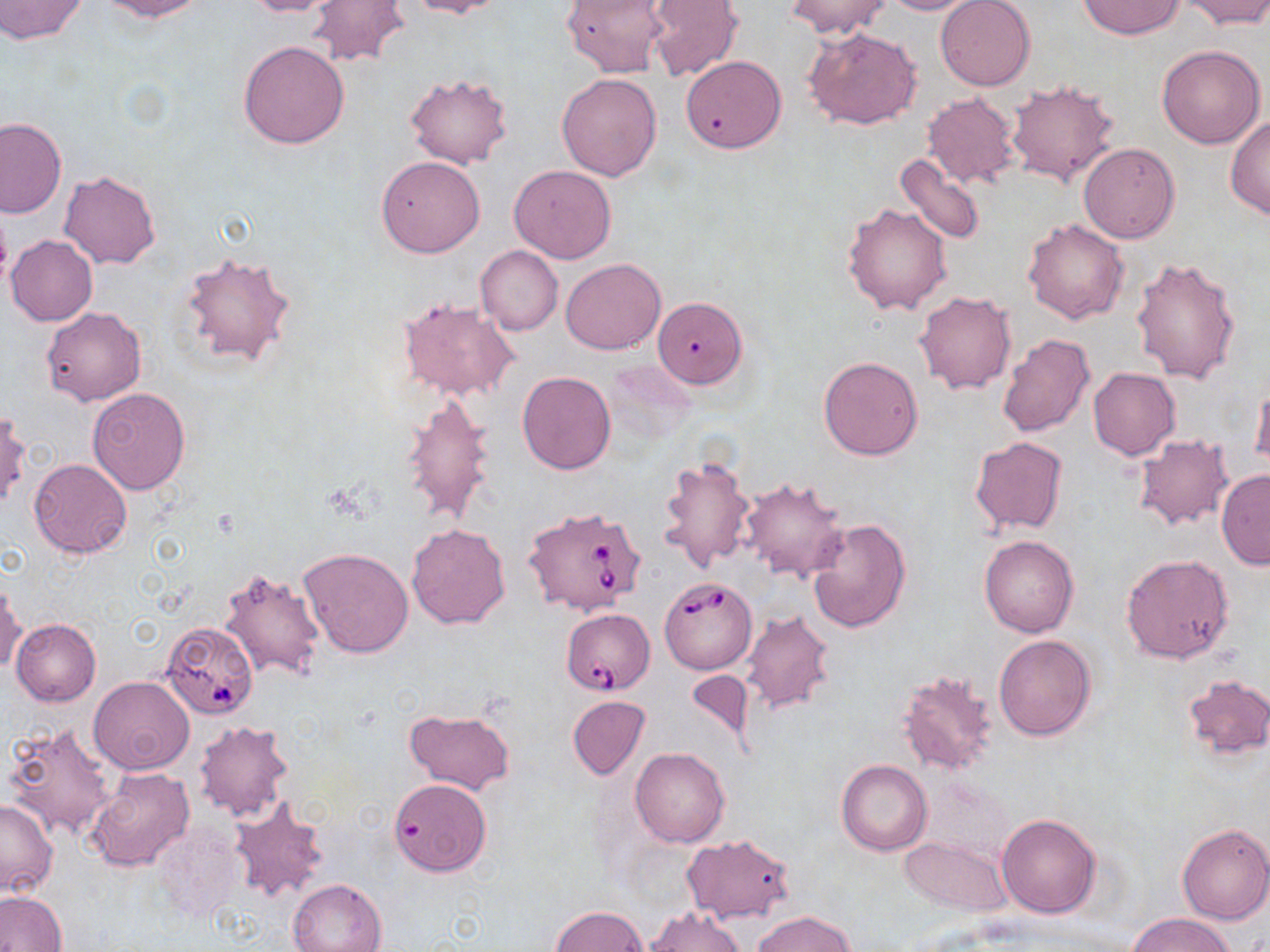

Summary:
  - Coordinate format: approximate bounding boxes as [x1, y1, x2, y2] in pixels
  - Uninfected red blood cell locations: [0, 0, 88, 44], [97, 0, 207, 21], [242, 0, 345, 17], [308, 0, 409, 67], [401, 0, 508, 19], [562, 0, 670, 77], [787, 0, 890, 38], [878, 0, 982, 14], [935, 0, 1036, 91], [1077, 0, 1185, 38], [1182, 0, 1270, 28], [645, 1, 743, 80], [805, 26, 922, 131], [237, 40, 350, 148], [1157, 45, 1265, 149], [680, 55, 786, 154], [557, 72, 663, 180], [405, 73, 514, 169], [1007, 79, 1121, 190], [921, 93, 1023, 189], [1227, 116, 1270, 221], [0, 118, 66, 218], [1079, 143, 1180, 242], [894, 151, 988, 246], [376, 156, 485, 257], [509, 164, 616, 263], [59, 171, 161, 269], [0, 202, 11, 294], [844, 203, 952, 315], [1022, 219, 1129, 324], [6, 235, 97, 326], [476, 246, 563, 335], [177, 250, 298, 371], [1131, 257, 1241, 384], [561, 259, 665, 354], [914, 291, 1017, 395], [397, 296, 519, 402], [656, 299, 750, 390], [41, 307, 146, 406], [996, 333, 1094, 438], [817, 356, 924, 461], [1088, 368, 1180, 460], [517, 371, 616, 474], [1251, 380, 1270, 474], [87, 388, 190, 494], [402, 394, 498, 527], [1, 410, 29, 512], [1133, 435, 1234, 532], [969, 436, 1069, 537], [654, 453, 758, 574], [29, 459, 132, 558], [1216, 471, 1269, 567], [740, 476, 850, 584], [805, 517, 912, 634], [406, 522, 512, 629], [978, 535, 1079, 637], [298, 546, 415, 658], [1120, 553, 1236, 664], [217, 566, 327, 680], [1, 579, 25, 676], [741, 611, 834, 715], [12, 619, 101, 706], [993, 634, 1096, 741], [683, 671, 756, 749], [898, 671, 1000, 779], [1182, 673, 1270, 760], [89, 676, 193, 774], [567, 695, 649, 779], [404, 708, 516, 795], [194, 719, 292, 822], [3, 721, 120, 842], [630, 746, 731, 847], [836, 759, 932, 855], [84, 765, 194, 873], [389, 778, 492, 877], [0, 799, 58, 897], [227, 800, 330, 904], [997, 814, 1101, 918], [153, 822, 242, 926], [1177, 823, 1270, 925], [681, 834, 795, 924], [899, 835, 1014, 916], [287, 879, 388, 951], [0, 890, 67, 952], [645, 905, 746, 951], [550, 906, 648, 951], [753, 910, 855, 952], [1128, 912, 1237, 952]
  - Babesia divergens-infected red blood cell locations: [522, 507, 649, 618], [658, 576, 757, 674], [560, 609, 655, 695], [160, 621, 259, 720]
  - Slide-level diagnosis: Babesia divergens
  - Modality: light microscopy
  - Preparation: thin blood film
  - Field of view: one of a larger specimen
  - Image size: 1270×952 pixels
  - Magnification: 1000x
  - Stain: May-Grünwald-Giemsa